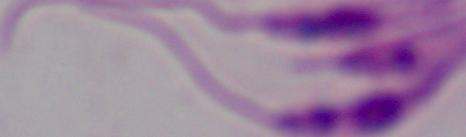

Summary:
  - Modality: micrograph
  - Identification: Leishmania
  - Magnification: 1000x